Assess the morphology of the red blood cells.
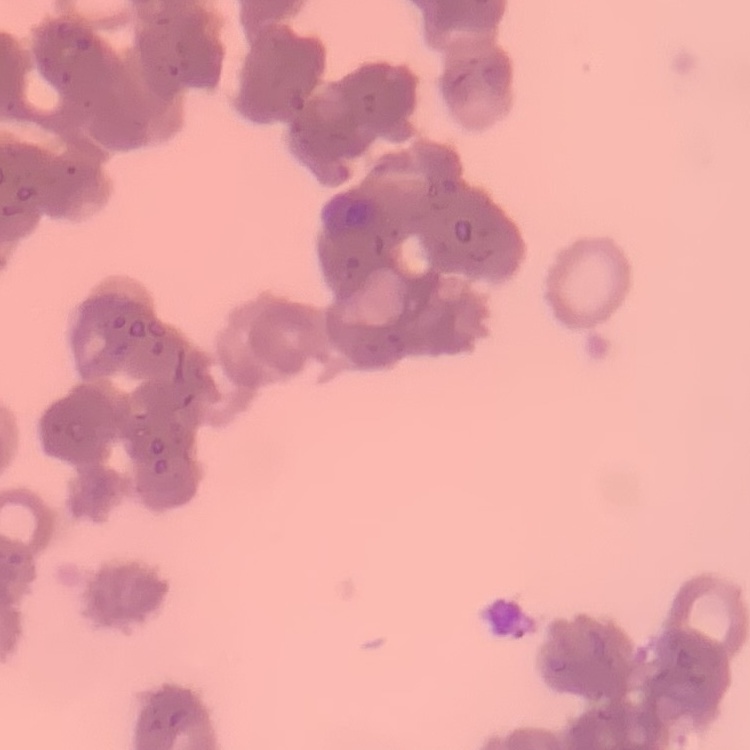
Rouleaux formation.

Square crop of a larger photomicrograph. Thin blood smear. Field's or Giemsa stain.